Name the blood parasite species.
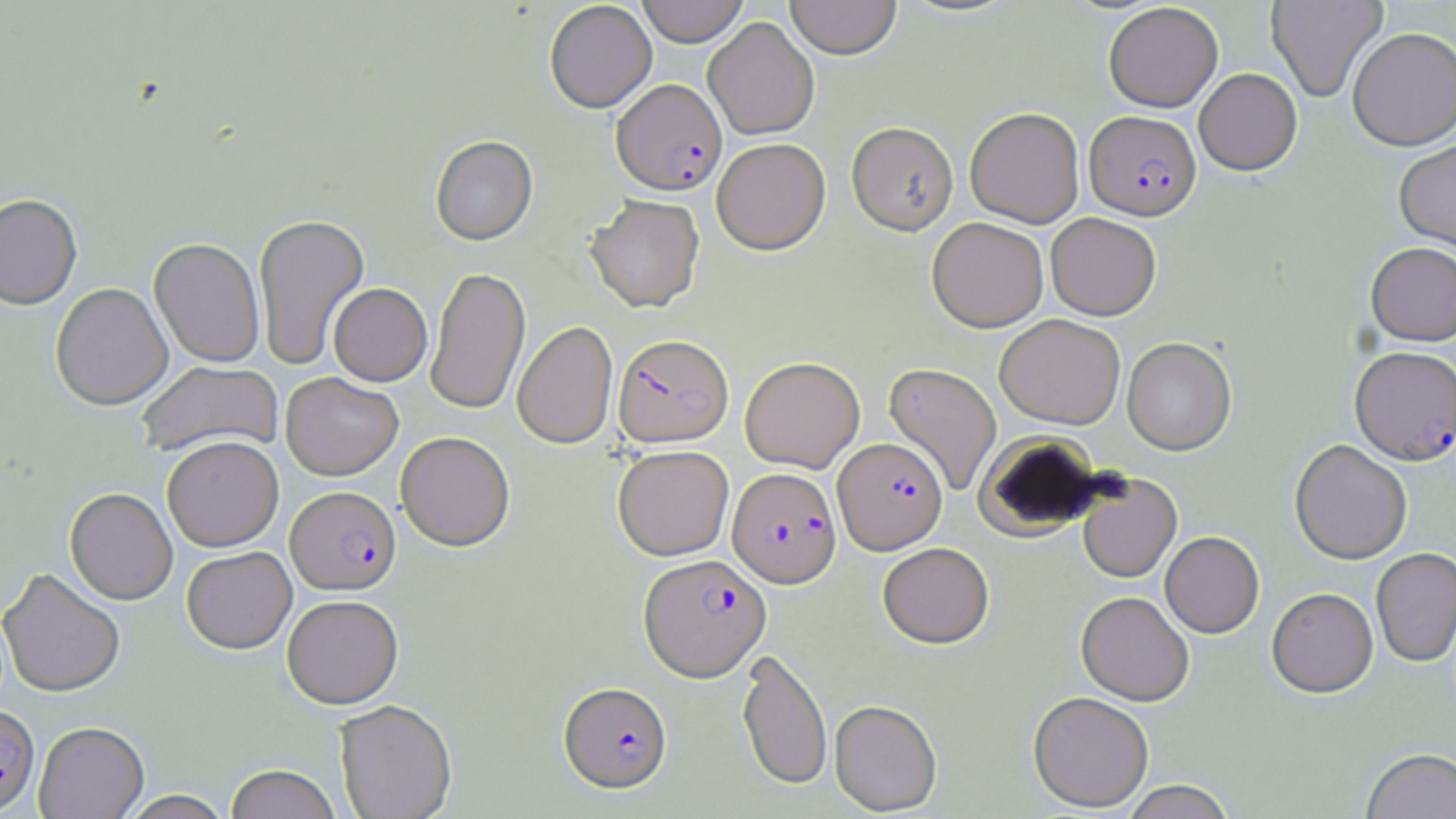
Plasmodium falciparum.

{
  "magnification": "1000x",
  "modality": "light microscopy",
  "uninfected_red_blood_cell_locations": "approximate bounding boxes as (x1, y1, x2, y2) in pixels: (636, 0, 749, 47), (785, 0, 902, 60), (1266, 0, 1387, 102), (544, 2, 657, 114), (1103, 3, 1223, 112), (703, 17, 819, 140), (1347, 27, 1456, 151), (1194, 68, 1302, 175), (965, 107, 1085, 228), (846, 123, 958, 236), (430, 136, 538, 247), (711, 139, 830, 255), (1395, 139, 1456, 257), (0, 194, 83, 310), (585, 196, 705, 313), (1046, 213, 1161, 320), (254, 214, 369, 371), (927, 218, 1048, 332), (149, 239, 265, 368), (1365, 242, 1456, 346), (426, 267, 530, 414), (50, 282, 173, 411), (328, 283, 432, 386), (995, 314, 1125, 429), (512, 321, 618, 450), (1122, 338, 1236, 456), (740, 356, 864, 473), (138, 361, 283, 458), (883, 363, 1002, 496), (280, 373, 403, 481), (396, 431, 515, 552), (163, 436, 284, 551), (1290, 439, 1412, 564), (612, 445, 734, 561), (1077, 475, 1182, 584), (64, 488, 178, 604), (1160, 531, 1264, 638), (878, 542, 994, 649), (182, 547, 296, 654), (1371, 547, 1456, 668), (0, 567, 126, 697), (1267, 588, 1378, 698), (1076, 592, 1194, 706), (282, 596, 404, 709), (737, 650, 832, 790), (1028, 691, 1154, 812), (829, 699, 942, 815), (334, 701, 457, 819), (34, 722, 148, 819), (1360, 747, 1456, 819), (224, 765, 342, 819), (1120, 780, 1236, 819), (118, 790, 235, 819)",
  "image_size": "1456×819 pixels",
  "plasmodium_falciparum_infected_red_blood_cell_locations": "approximate bounding boxes as (x1, y1, x2, y2) in pixels: (611, 79, 727, 197), (1084, 111, 1201, 220), (612, 334, 734, 448), (1350, 346, 1456, 466), (833, 438, 947, 555), (727, 468, 842, 589), (285, 486, 401, 595), (638, 554, 771, 682), (559, 682, 672, 794), (0, 705, 40, 815)",
  "field_of_view": "one of a larger specimen",
  "preparation": "thin blood film",
  "stain": "May-Grünwald-Giemsa"
}